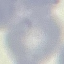
Result: no malaria parasites seen. Acquired by smartphone through the microscope eyepiece. Automatically extracted cell patch, resized to 64 × 64 pixels. Giemsa-stained preparation. Thin smear of blood.